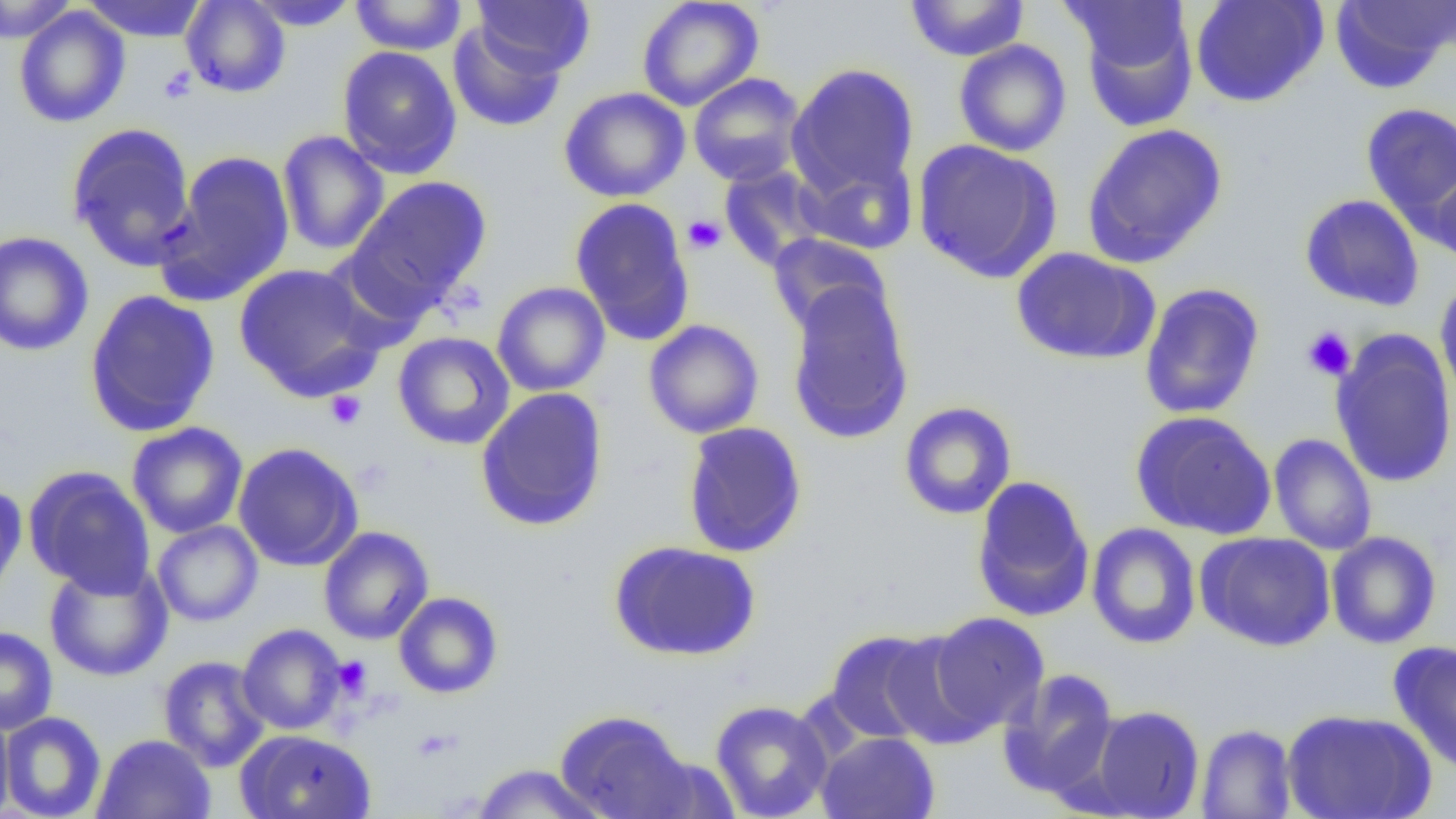

slide_level_diagnosis: no evidence of blood parasites
field_of_view: one of a larger specimen
image_size: 1456×819 pixels
platelet_locations: 'approximate bounding boxes as (x1, y1, x2, y2) in pixels: (158, 66, 197, 103), (683, 215, 726, 254), (1302, 326, 1356, 381), (325, 390, 367, 430), (332, 656, 372, 697)'
modality: optical microscopy
magnification: 1000x
uninfected_red_blood_cell_locations: 'approximate bounding boxes as (x1, y1, x2, y2) in pixels: (0, 0, 77, 43), (81, 0, 209, 42), (181, 0, 290, 98), (349, 0, 467, 55), (472, 0, 596, 77), (637, 0, 764, 111), (1190, 0, 1328, 108), (1329, 0, 1454, 92), (247, 1, 359, 31), (905, 1, 1030, 61), (1077, 5, 1198, 133), (13, 6, 130, 128), (447, 22, 566, 132), (953, 40, 1072, 157), (337, 46, 462, 179), (786, 63, 920, 200), (688, 73, 806, 187), (558, 86, 690, 203), (1361, 102, 1456, 227), (66, 122, 197, 270), (1081, 122, 1228, 268), (277, 130, 390, 256), (912, 139, 1063, 284), (158, 150, 296, 305), (798, 153, 919, 256), (1427, 163, 1456, 270), (718, 165, 830, 271), (345, 175, 492, 315), (1299, 193, 1425, 312), (570, 197, 696, 346), (0, 230, 94, 357), (767, 233, 892, 339), (1011, 247, 1159, 365), (233, 263, 382, 400), (1435, 277, 1456, 408), (492, 281, 610, 397), (784, 282, 914, 444), (1139, 283, 1265, 419), (84, 290, 221, 437), (643, 319, 765, 439), (1330, 329, 1456, 489), (393, 332, 515, 450), (475, 387, 609, 530), (899, 401, 1017, 520), (1130, 410, 1277, 540), (682, 421, 808, 558), (127, 422, 247, 539), (1268, 433, 1377, 555), (232, 442, 363, 571), (24, 465, 156, 597), (971, 475, 1095, 623), (0, 483, 28, 606), (152, 520, 263, 627), (1086, 522, 1201, 650), (319, 526, 434, 644), (1196, 531, 1335, 651), (1326, 531, 1442, 649), (609, 540, 761, 662), (43, 561, 173, 681), (393, 592, 503, 699), (927, 611, 1049, 736), (237, 623, 346, 735), (0, 626, 58, 736), (824, 629, 952, 745), (1388, 640, 1456, 777), (158, 655, 271, 772), (998, 668, 1120, 800), (710, 700, 832, 819), (1087, 704, 1205, 817), (1281, 708, 1436, 819), (0, 709, 15, 818), (555, 709, 698, 819), (0, 711, 107, 818), (1195, 723, 1297, 818), (235, 729, 377, 819), (815, 731, 940, 819), (92, 734, 216, 819), (468, 762, 611, 818)'
preparation: thin blood film